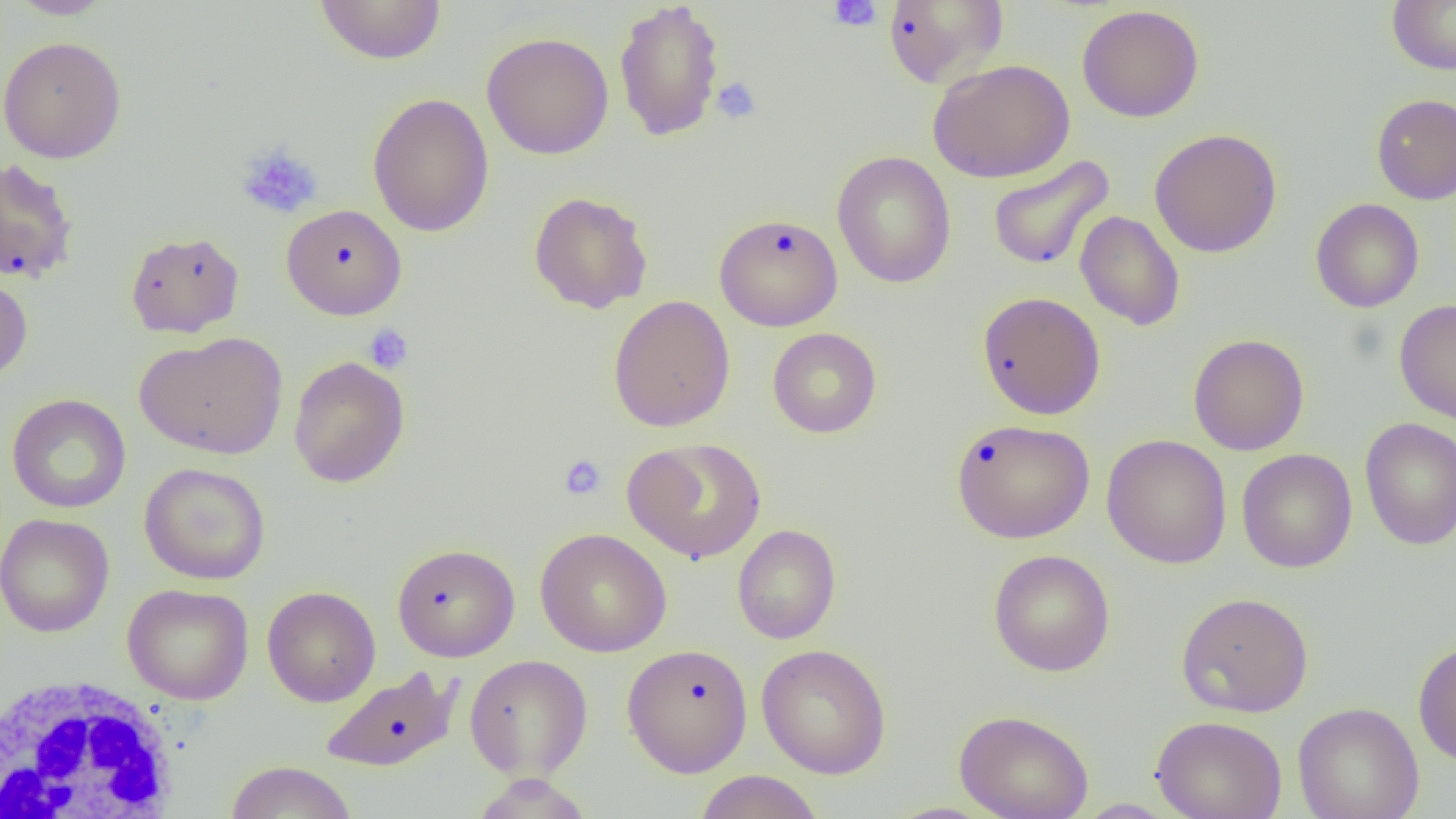 Approximate bounding boxes as named x1/y1/x2/y2 corners in pixels. White blood cell locations: (x1=0, y1=674, x2=182, y2=818). Platelet locations: (x1=827, y1=1, x2=883, y2=32), (x1=710, y1=77, x2=762, y2=125), (x1=236, y1=142, x2=324, y2=219), (x1=364, y1=324, x2=413, y2=374), (x1=558, y1=454, x2=607, y2=501). Uninfected red blood cell locations: (x1=6, y1=0, x2=115, y2=19), (x1=314, y1=0, x2=447, y2=66), (x1=613, y1=0, x2=726, y2=142), (x1=1387, y1=0, x2=1456, y2=75), (x1=881, y1=1, x2=1009, y2=88), (x1=1077, y1=4, x2=1205, y2=123), (x1=481, y1=32, x2=614, y2=160), (x1=0, y1=36, x2=127, y2=163), (x1=926, y1=58, x2=1076, y2=183), (x1=367, y1=93, x2=495, y2=238), (x1=1371, y1=93, x2=1456, y2=205), (x1=1149, y1=128, x2=1283, y2=258), (x1=831, y1=151, x2=957, y2=288), (x1=987, y1=155, x2=1115, y2=271), (x1=0, y1=157, x2=80, y2=284), (x1=528, y1=191, x2=653, y2=314), (x1=1310, y1=198, x2=1424, y2=313), (x1=281, y1=204, x2=407, y2=320), (x1=1075, y1=211, x2=1185, y2=331), (x1=714, y1=213, x2=843, y2=331), (x1=125, y1=231, x2=245, y2=338), (x1=0, y1=270, x2=33, y2=382), (x1=977, y1=291, x2=1106, y2=419), (x1=608, y1=294, x2=736, y2=432), (x1=1394, y1=299, x2=1456, y2=424), (x1=767, y1=327, x2=882, y2=438), (x1=135, y1=331, x2=288, y2=459), (x1=1187, y1=333, x2=1309, y2=456), (x1=288, y1=356, x2=410, y2=488), (x1=6, y1=394, x2=131, y2=514), (x1=951, y1=418, x2=1095, y2=543), (x1=1359, y1=418, x2=1456, y2=551), (x1=1102, y1=434, x2=1232, y2=569), (x1=624, y1=437, x2=766, y2=564), (x1=1236, y1=449, x2=1357, y2=573), (x1=139, y1=462, x2=271, y2=585), (x1=0, y1=513, x2=114, y2=637), (x1=732, y1=524, x2=841, y2=644), (x1=535, y1=527, x2=672, y2=657), (x1=392, y1=542, x2=520, y2=662), (x1=988, y1=549, x2=1115, y2=676), (x1=122, y1=583, x2=255, y2=705), (x1=262, y1=586, x2=380, y2=707), (x1=1175, y1=592, x2=1314, y2=717), (x1=1412, y1=640, x2=1456, y2=767), (x1=622, y1=643, x2=753, y2=777), (x1=756, y1=644, x2=892, y2=779), (x1=464, y1=654, x2=593, y2=781), (x1=320, y1=666, x2=462, y2=772), (x1=1293, y1=702, x2=1424, y2=819), (x1=954, y1=709, x2=1094, y2=819), (x1=1150, y1=715, x2=1287, y2=819), (x1=224, y1=761, x2=358, y2=819), (x1=694, y1=770, x2=824, y2=819), (x1=470, y1=774, x2=593, y2=819), (x1=1073, y1=798, x2=1178, y2=818). Slide-level diagnosis: negative for blood parasites. 1000x magnification. Image is 1456×819 pixels. Light microscopy. Single field of view. Thin blood smear.